Locate every blood parasite and identify its species.
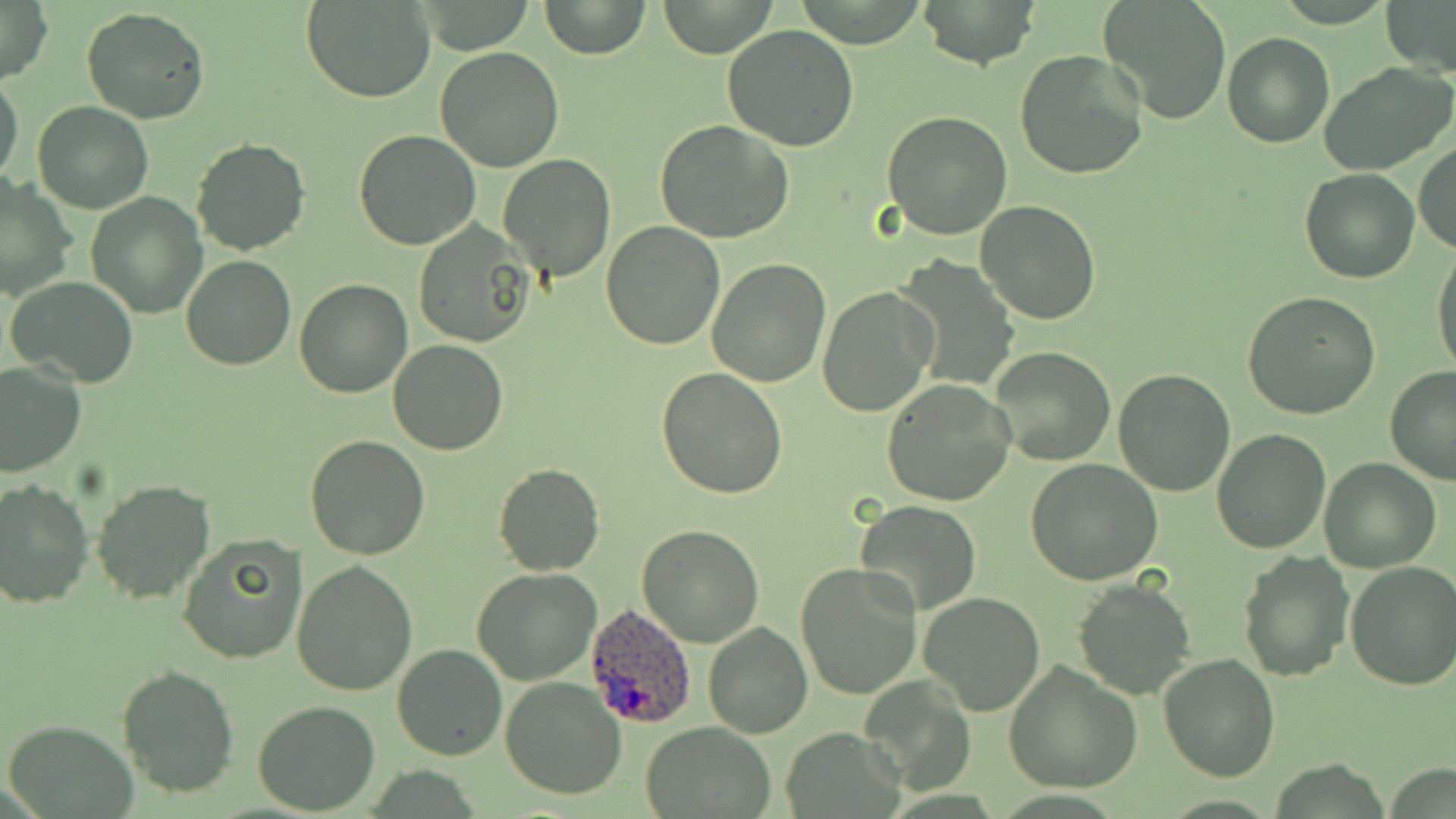

Approximate bounding boxes as (x1,y1)-(x2,y2) corner pairs in pixels.
Plasmodium ovale-infected red blood cells: (586,604)-(698,730).
No Plasmodium falciparum, Plasmodium malariae, Plasmodium vivax, Babesia divergens, or Trypanosoma brucei observed.

Uninfected red blood cell locations: (538,0)-(651,59), (656,0)-(778,57), (914,0)-(1041,70), (1098,0)-(1230,123), (1382,0)-(1456,78), (0,1)-(53,85), (304,1)-(437,103), (81,7)-(210,125), (721,24)-(861,152), (1223,31)-(1333,148), (435,46)-(565,171), (1014,47)-(1148,180), (1319,61)-(1455,176), (0,74)-(24,187), (33,102)-(153,214), (881,110)-(1013,240), (655,121)-(794,244), (354,130)-(480,249), (190,137)-(309,256), (1413,143)-(1455,255), (499,153)-(614,280), (1299,167)-(1420,284), (1,175)-(76,302), (86,190)-(208,317), (976,201)-(1101,325), (411,222)-(535,348), (602,222)-(726,352), (1431,244)-(1456,382), (183,255)-(295,371), (897,257)-(1020,388), (708,259)-(830,388), (6,274)-(140,387), (294,280)-(413,399), (816,286)-(940,416), (1241,291)-(1381,420), (388,340)-(508,455), (986,346)-(1115,466), (0,362)-(86,478), (1384,366)-(1456,484), (656,367)-(788,499), (1113,369)-(1236,497), (882,377)-(1016,505), (1211,428)-(1330,554), (305,435)-(432,560), (1317,457)-(1441,573), (1026,459)-(1163,585), (494,463)-(604,576), (1,478)-(94,608), (90,480)-(216,603), (855,501)-(982,615), (638,524)-(763,646), (177,535)-(306,663), (1238,548)-(1356,682), (292,561)-(419,697), (795,562)-(923,699), (1345,562)-(1456,691), (471,566)-(601,685), (1072,579)-(1196,701), (918,591)-(1046,715), (703,619)-(813,738), (391,643)-(508,762), (1159,653)-(1279,782), (1004,658)-(1141,792), (115,663)-(239,799), (861,674)-(974,793), (501,677)-(626,801), (252,701)-(381,815), (0,718)-(141,819), (641,721)-(776,817), (781,726)-(907,818). Slide-level diagnosis: Plasmodium ovale. Captured at 1000x magnification. Light microscopy. Thin blood film. Image is 1456×819 pixels. May-Grünwald-Giemsa-stained preparation. Single field of view.